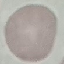

Summary:
  - Malaria status: uninfected
  - Capture: smartphone camera at the microscope eyepiece
  - Stain: Giemsa
  - Preparation: thin blood film
  - Image type: automatically extracted cell patch, resized to 64 × 64 pixels